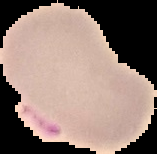
Segmented cell region on a black background. Image is 157×154 pixels. From a thin blood smear. Result: Plasmodium parasites identified.